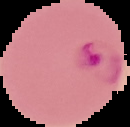 From a thin blood film. Malaria status: parasitized. Segmented cell region on a black background. Image is 130×127 pixels.